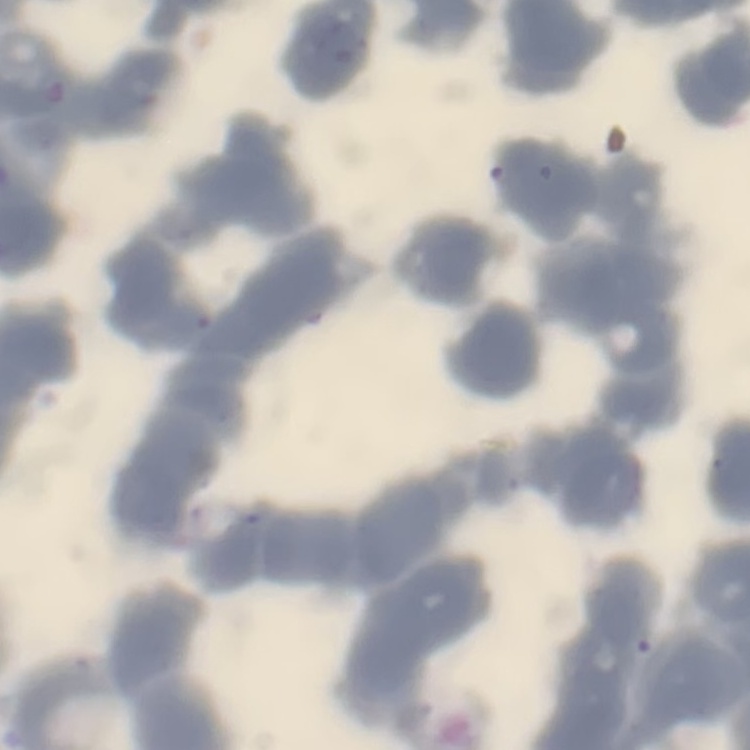
The red blood cells show rouleaux formation. Square crop of a larger photomicrograph. Thin peripheral smear. Stained with either Field's or Giemsa.